Report the malaria status of this cell.
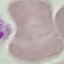
It is uninfected.

Summary:
  - Stain: Giemsa
  - Image type: cell patch, automatically extracted from a larger field of view and resized to 64 × 64 pixels
  - Preparation: thin blood film
  - Capture: smartphone through the microscope eyepiece